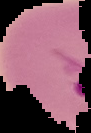 Segmented cell region on a black background. Image is 91×133 pixels. Malaria status: parasitized. From a thin blood film.